Comment on the morphology of the erythrocytes.
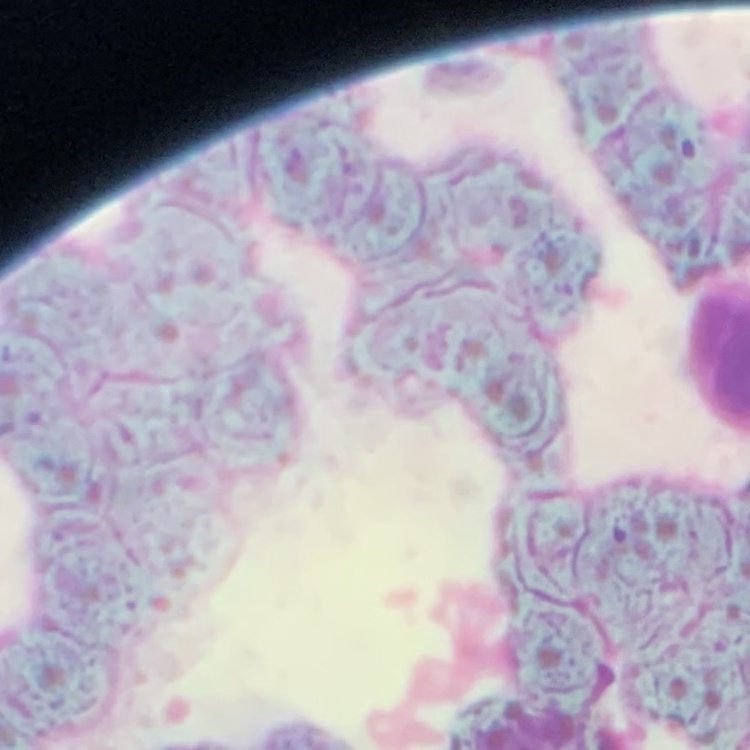

Rouleaux formation.

{
  "preparation": "thin blood smear",
  "stain": "Field's or Giemsa",
  "image_type": "one tile cut from a larger photomicrograph"
}